Identify the parasite.
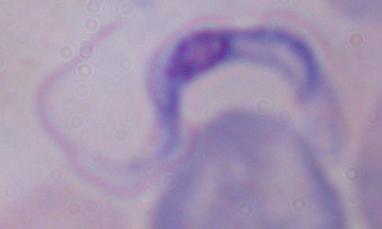

A trypanosome.

Summary:
  - Modality: photomicrograph
  - Magnification: 1000x